Report the malaria status of this cell.
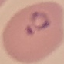

Parasitized.

Thin smear of blood. Giemsa-stained preparation. Cell patch, automatically extracted from a larger field of view and resized to 64 × 64 pixels. Acquired by smartphone through the microscope eyepiece.